Assess for malaria.
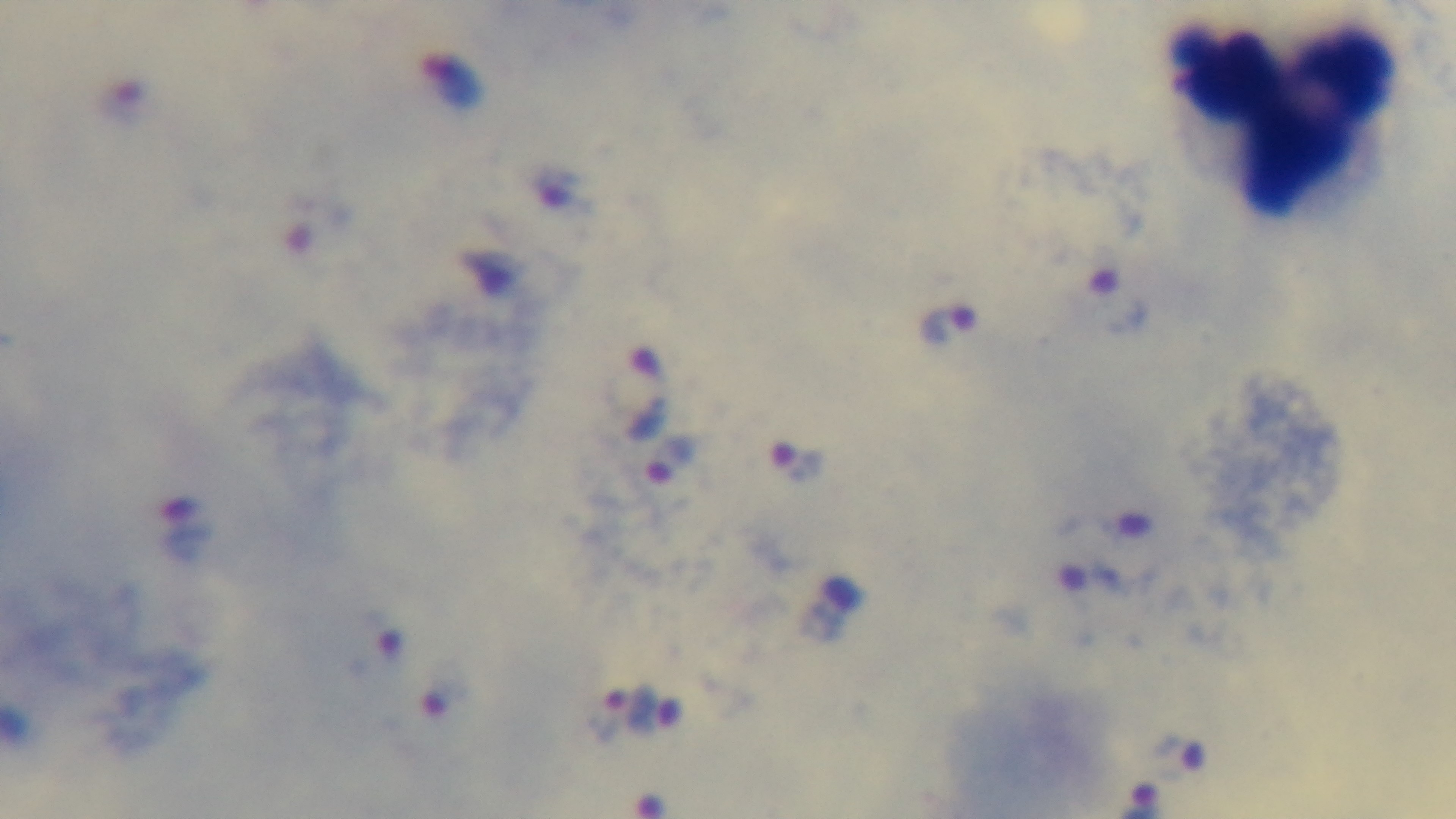

Infected.

Preparation: thick blood film. Oil-immersion objective, 100x. Photomicrograph. Single field of view. Giemsa-stained. Mounted 4K digital camera.